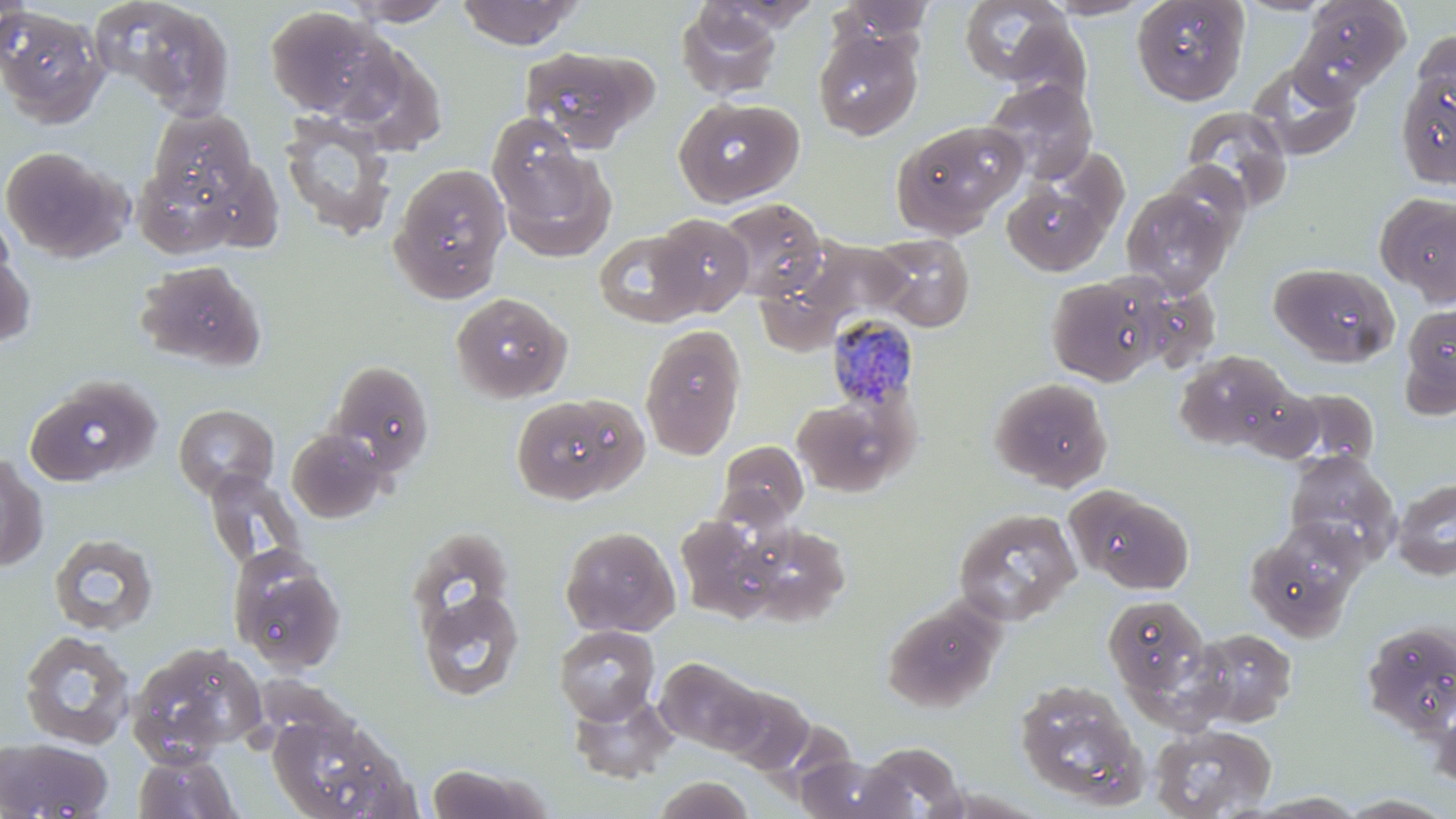

{
  "slide_level_diagnosis": "Plasmodium malariae",
  "field_of_view": "one of a larger specimen",
  "plasmodium_malariae_infected_red_blood_cell_locations": "approximate bounding boxes as named x1/y1/x2/y2 corners in pixels: (x1=825, y1=313, x2=920, y2=411)",
  "modality": "optical microscopy",
  "magnification": "1000x",
  "image_size": "1456×819 pixels",
  "stain": "May-Grünwald-Giemsa",
  "preparation": "thin blood film",
  "uninfected_red_blood_cell_locations": "approximate bounding boxes as named x1/y1/x2/y2 corners in pixels: (x1=0, y1=0, x2=30, y2=65), (x1=97, y1=0, x2=238, y2=121), (x1=456, y1=0, x2=584, y2=50), (x1=1042, y1=0, x2=1153, y2=20), (x1=1131, y1=0, x2=1249, y2=105), (x1=1237, y1=0, x2=1336, y2=16), (x1=1294, y1=0, x2=1410, y2=97), (x1=342, y1=1, x2=458, y2=27), (x1=830, y1=1, x2=937, y2=50), (x1=958, y1=1, x2=1078, y2=87), (x1=676, y1=4, x2=784, y2=101), (x1=263, y1=6, x2=395, y2=120), (x1=0, y1=7, x2=108, y2=127), (x1=813, y1=27, x2=923, y2=140), (x1=1412, y1=29, x2=1456, y2=121), (x1=340, y1=41, x2=447, y2=156), (x1=516, y1=45, x2=658, y2=152), (x1=1248, y1=59, x2=1361, y2=160), (x1=1396, y1=67, x2=1455, y2=189), (x1=983, y1=78, x2=1098, y2=184), (x1=674, y1=97, x2=804, y2=207), (x1=1180, y1=106, x2=1294, y2=215), (x1=148, y1=109, x2=258, y2=202), (x1=277, y1=112, x2=397, y2=240), (x1=487, y1=114, x2=593, y2=221), (x1=890, y1=120, x2=1026, y2=238), (x1=494, y1=141, x2=617, y2=261), (x1=0, y1=145, x2=126, y2=262), (x1=132, y1=161, x2=245, y2=259), (x1=1159, y1=161, x2=1252, y2=249), (x1=389, y1=162, x2=511, y2=302), (x1=1000, y1=179, x2=1113, y2=277), (x1=1122, y1=187, x2=1234, y2=296), (x1=1374, y1=192, x2=1456, y2=304), (x1=717, y1=197, x2=829, y2=303), (x1=651, y1=213, x2=754, y2=318), (x1=593, y1=230, x2=705, y2=328), (x1=873, y1=234, x2=975, y2=332), (x1=0, y1=236, x2=35, y2=351), (x1=800, y1=240, x2=913, y2=325), (x1=134, y1=259, x2=267, y2=372), (x1=1270, y1=262, x2=1399, y2=366), (x1=1045, y1=273, x2=1167, y2=387), (x1=450, y1=291, x2=572, y2=403), (x1=1398, y1=301, x2=1456, y2=418), (x1=639, y1=324, x2=746, y2=460), (x1=1172, y1=349, x2=1299, y2=453), (x1=327, y1=360, x2=436, y2=477), (x1=25, y1=374, x2=162, y2=488), (x1=989, y1=377, x2=1113, y2=491), (x1=1277, y1=387, x2=1381, y2=472), (x1=511, y1=393, x2=646, y2=506), (x1=792, y1=396, x2=907, y2=497), (x1=173, y1=404, x2=279, y2=500), (x1=285, y1=428, x2=391, y2=523), (x1=718, y1=439, x2=808, y2=526), (x1=1283, y1=449, x2=1401, y2=565), (x1=0, y1=451, x2=48, y2=573), (x1=202, y1=468, x2=306, y2=573), (x1=1392, y1=477, x2=1456, y2=580), (x1=1066, y1=484, x2=1195, y2=594), (x1=953, y1=508, x2=1081, y2=626), (x1=673, y1=513, x2=780, y2=621), (x1=1245, y1=523, x2=1364, y2=641), (x1=746, y1=524, x2=851, y2=624), (x1=560, y1=525, x2=681, y2=637), (x1=407, y1=528, x2=516, y2=640), (x1=48, y1=533, x2=159, y2=637), (x1=228, y1=548, x2=347, y2=675), (x1=417, y1=588, x2=525, y2=702), (x1=1103, y1=594, x2=1212, y2=702), (x1=880, y1=597, x2=1005, y2=713), (x1=1360, y1=620, x2=1456, y2=739), (x1=554, y1=625, x2=660, y2=723), (x1=1192, y1=627, x2=1298, y2=727), (x1=18, y1=630, x2=135, y2=750), (x1=127, y1=639, x2=268, y2=763), (x1=655, y1=656, x2=764, y2=756), (x1=1014, y1=678, x2=1148, y2=809), (x1=719, y1=685, x2=814, y2=775), (x1=567, y1=691, x2=679, y2=783), (x1=1431, y1=697, x2=1456, y2=792), (x1=266, y1=708, x2=417, y2=819), (x1=1149, y1=723, x2=1277, y2=818), (x1=0, y1=735, x2=114, y2=818), (x1=860, y1=742, x2=968, y2=818), (x1=132, y1=750, x2=242, y2=819), (x1=799, y1=754, x2=907, y2=819), (x1=425, y1=763, x2=552, y2=819), (x1=652, y1=776, x2=754, y2=818), (x1=1243, y1=792, x2=1370, y2=817), (x1=1337, y1=793, x2=1456, y2=818)"
}